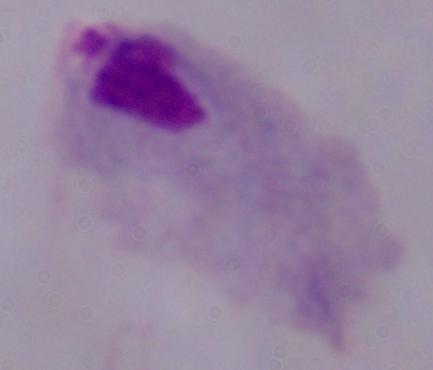
Summary:
  - Magnification: 1000x
  - Identification: trichomonad
  - Modality: photomicrograph